Comment on the morphology of the red blood cells.
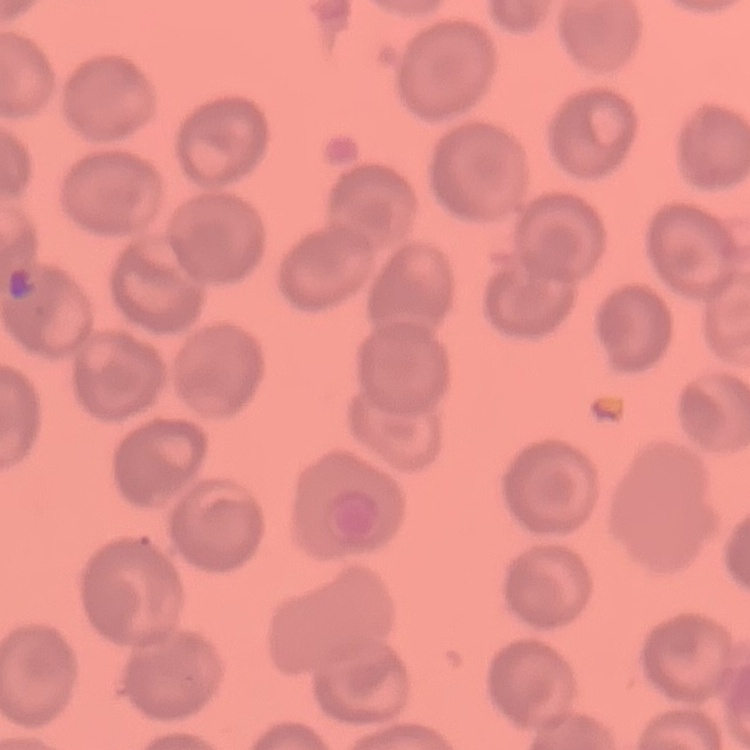

No rouleaux formation.

Summary:
  - Preparation: thin blood film
  - Image type: square crop of a larger photomicrograph
  - Stain: Field's or Giemsa